Classify this cell by malaria status.
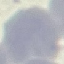
It is uninfected.

Automatically extracted cell patch, resized to 64 × 64 pixels. Photographed with a smartphone camera at the microscope eyepiece. Giemsa-stained preparation. Thin blood smear.